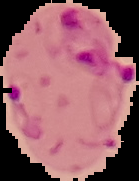
Summary:
  - Image type: segmented cell region with the area outside set to black
  - Preparation: thin blood smear
  - Malaria status: parasitized
  - Image size: 139×181 pixels